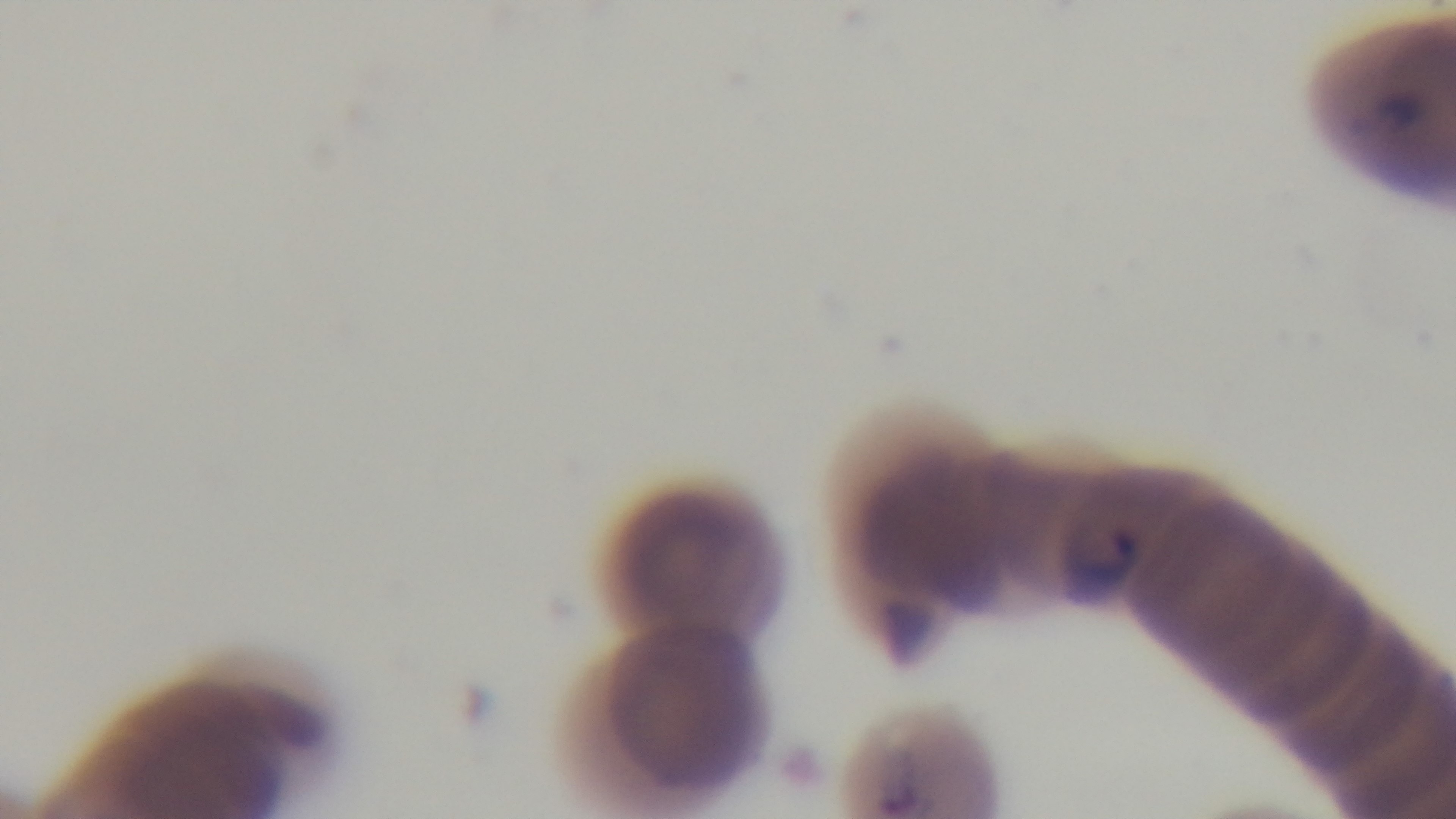
modality = light microscopy
field of view = one from the slide
objective = 100x oil immersion
capture = mounted 4K digital camera
malaria status = positive
preparation = thin blood film
stain = Giemsa